Assess this cell for malaria.
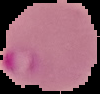
It is parasitized.

image size = 100×94 pixels
preparation = thin blood film
image type = segmented cell region with the area outside set to black